Describe the morphology of the erythrocytes.
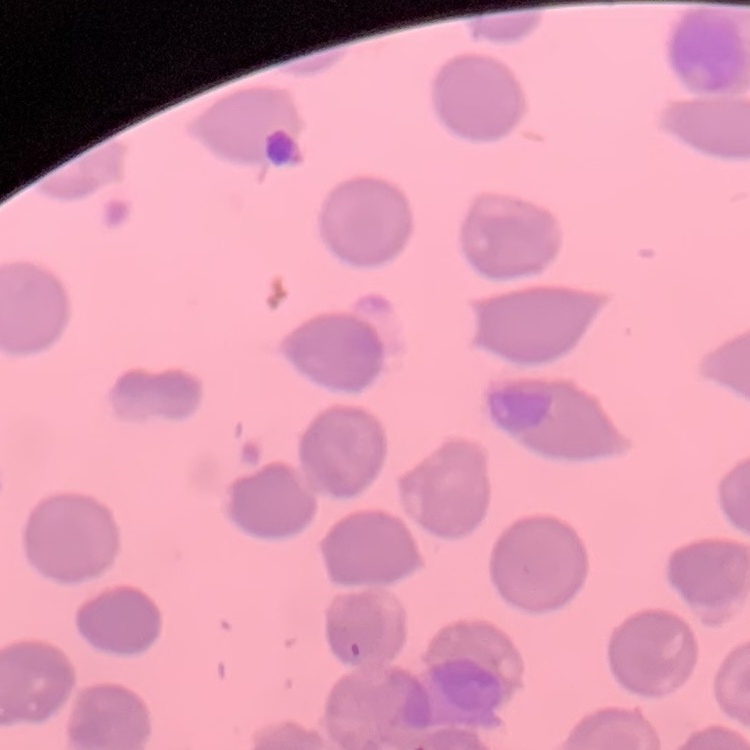
No rouleaux formation.

Summary:
  - Preparation: thin peripheral smear
  - Stain: Field's or Giemsa
  - Image type: square crop of a larger photomicrograph